Give the position of every malaria parasite and every leukocyte.
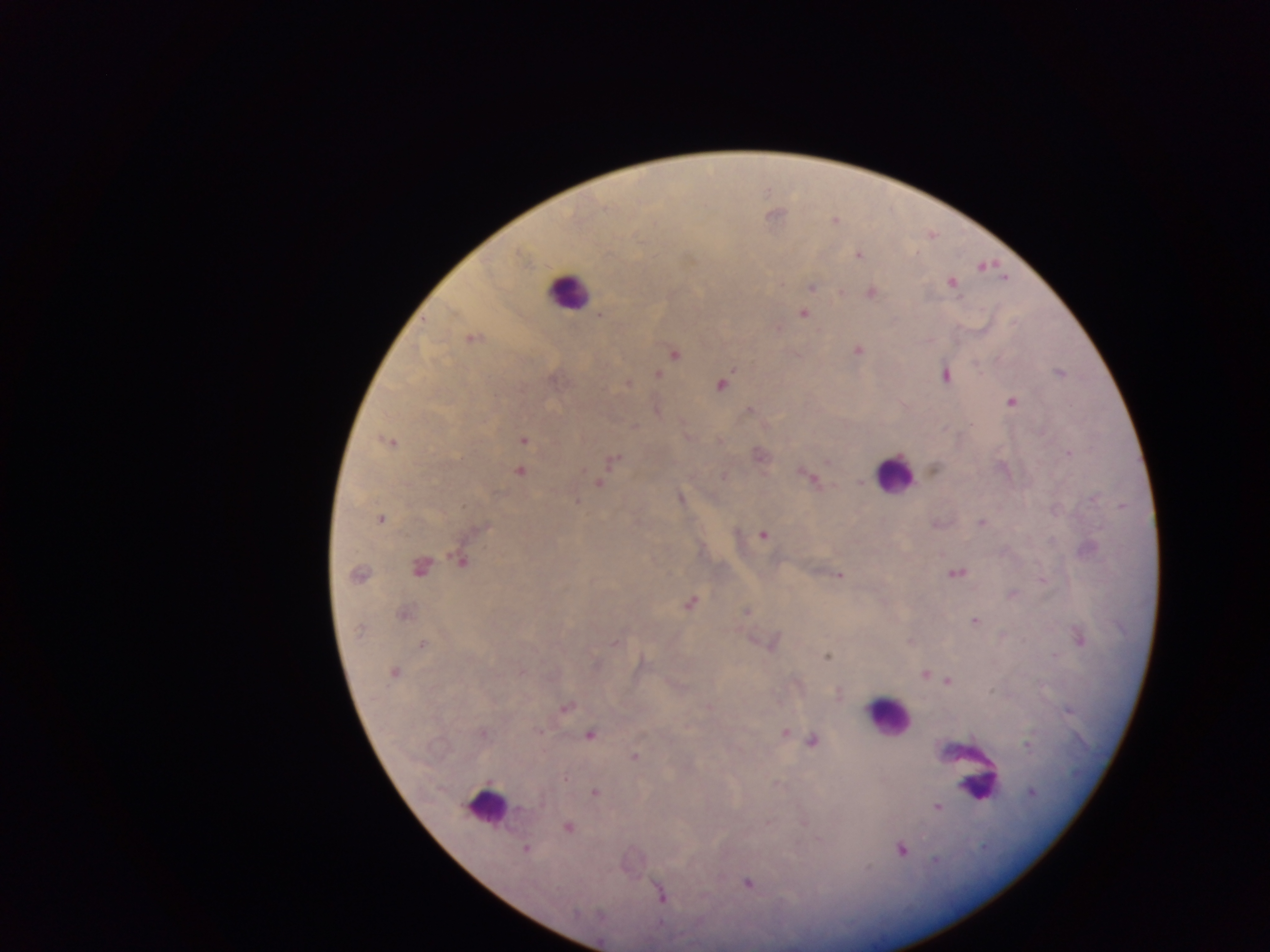

Approximate centers as (x, y) in pixels.
Malaria parasites: (835, 221), (858, 256), (981, 267), (952, 283), (812, 287), (871, 293), (803, 314), (600, 316), (471, 339), (857, 350), (674, 355), (658, 374), (1059, 374), (945, 375), (629, 383), (721, 385), (1012, 402), (749, 411), (523, 440), (389, 443), (1068, 453), (613, 461), (827, 462), (520, 471), (724, 477), (809, 478), (599, 483), (860, 483), (681, 498), (1093, 500), (577, 502), (381, 519), (981, 522), (481, 528), (764, 535), (461, 561), (419, 567), (956, 573), (358, 575), (839, 575), (1013, 595), (690, 603), (747, 611), (404, 613), (975, 620), (360, 631), (1079, 638), (615, 642), (422, 645), (827, 657), (393, 673), (522, 673), (924, 675), (949, 681), (837, 693), (566, 707), (539, 731), (785, 733), (483, 734), (591, 734), (812, 740), (1027, 745), (634, 756), (564, 778), (595, 793), (1031, 793), (937, 807), (521, 808), (568, 828), (525, 849), (902, 850), (935, 861), (748, 883), (661, 896), (575, 914).
Leukocytes: (567, 292), (893, 475), (887, 716), (968, 769), (487, 805).

preparation: thick blood smear
capture: mobile-phone photograph through a microscope
country: Ghana
field_of_view: single
image_size: 1270×952 pixels